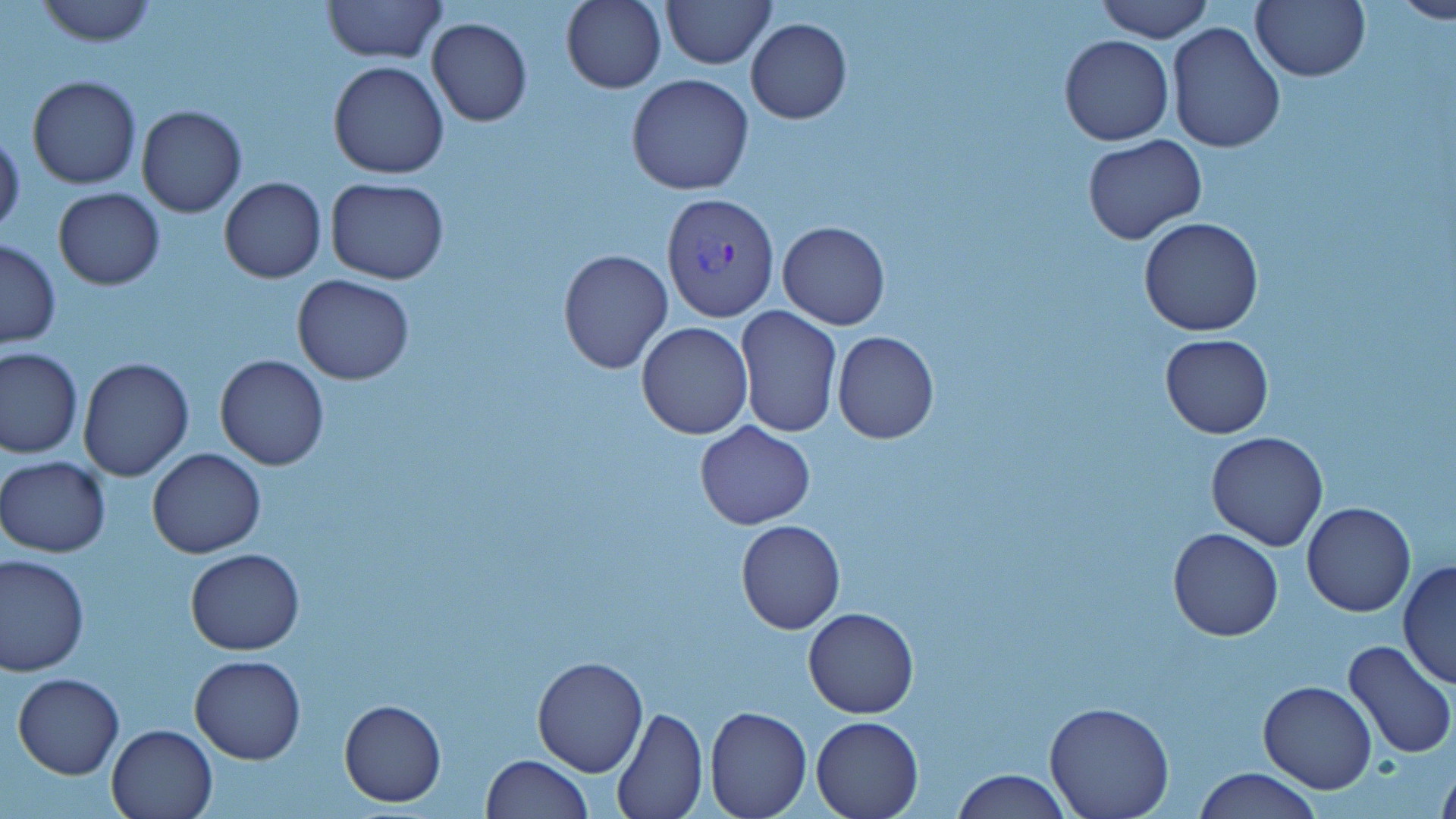
slide_level_diagnosis: Plasmodium vivax
image_size: 1456×819 pixels
preparation: thin blood smear
magnification: 1000x
modality: light microscopy
field_of_view: single
uninfected_red_blood_cell_locations: 'approximate bounding boxes as (x1, y1, x2, y2) in pixels: (323, 0, 445, 62), (561, 0, 667, 93), (662, 0, 775, 69), (1096, 0, 1216, 42), (1250, 0, 1369, 82), (1388, 0, 1456, 23), (31, 1, 160, 47), (427, 16, 532, 127), (746, 18, 851, 123), (1166, 24, 1284, 154), (1058, 35, 1174, 147), (328, 61, 449, 180), (625, 73, 754, 195), (26, 75, 141, 189), (135, 104, 247, 218), (0, 128, 25, 240), (1082, 135, 1207, 244), (219, 176, 326, 283), (324, 177, 450, 283), (53, 188, 165, 290), (1137, 217, 1265, 337), (777, 221, 890, 330), (0, 239, 61, 349), (556, 248, 673, 374), (292, 274, 414, 385), (734, 305, 841, 438), (636, 321, 754, 439), (832, 332, 940, 444), (1159, 334, 1274, 438), (1, 347, 83, 458), (215, 354, 329, 469), (76, 357, 193, 481), (695, 421, 815, 529), (1206, 431, 1329, 551), (147, 448, 266, 559), (1, 456, 110, 558), (1301, 502, 1416, 618), (735, 519, 845, 634), (1167, 527, 1284, 641), (185, 547, 304, 655), (1, 553, 91, 675), (1397, 559, 1456, 689), (803, 606, 918, 718), (1342, 640, 1455, 759), (190, 653, 307, 765), (532, 655, 647, 776), (11, 672, 124, 780), (1259, 679, 1377, 794), (339, 698, 448, 806), (1045, 700, 1175, 819), (704, 704, 812, 819), (612, 706, 707, 818), (811, 716, 923, 818), (106, 724, 217, 818), (480, 754, 593, 818), (1435, 755, 1456, 819), (1193, 767, 1322, 819), (950, 769, 1071, 819)'
stain: May-Grünwald-Giemsa
plasmodium_vivax_infected_red_blood_cell_locations: 'approximate bounding boxes as (x1, y1, x2, y2) in pixels: (659, 191, 779, 323)'